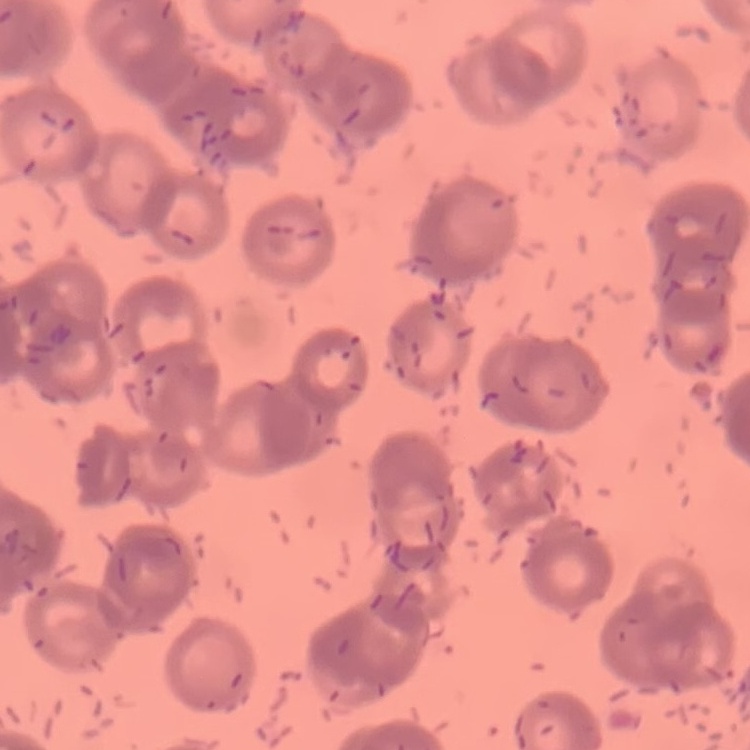
erythrocyte_morphology: rouleaux formation
stain: Field's or Giemsa
preparation: thin peripheral smear
image_type: one tile cut from a larger photomicrograph